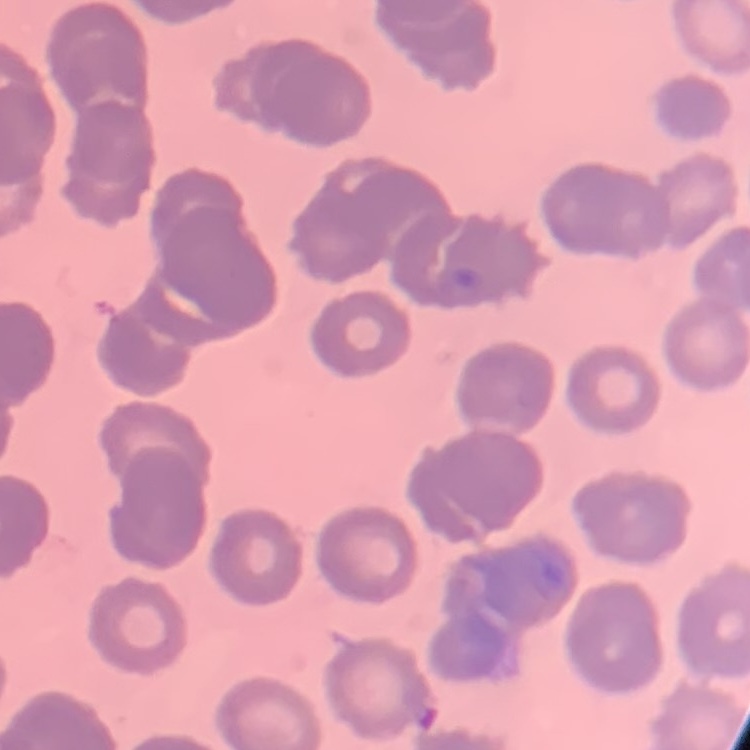
erythrocyte morphology = rouleaux formation
stain = Field's or Giemsa
preparation = thin blood film
image type = square crop of a larger photomicrograph